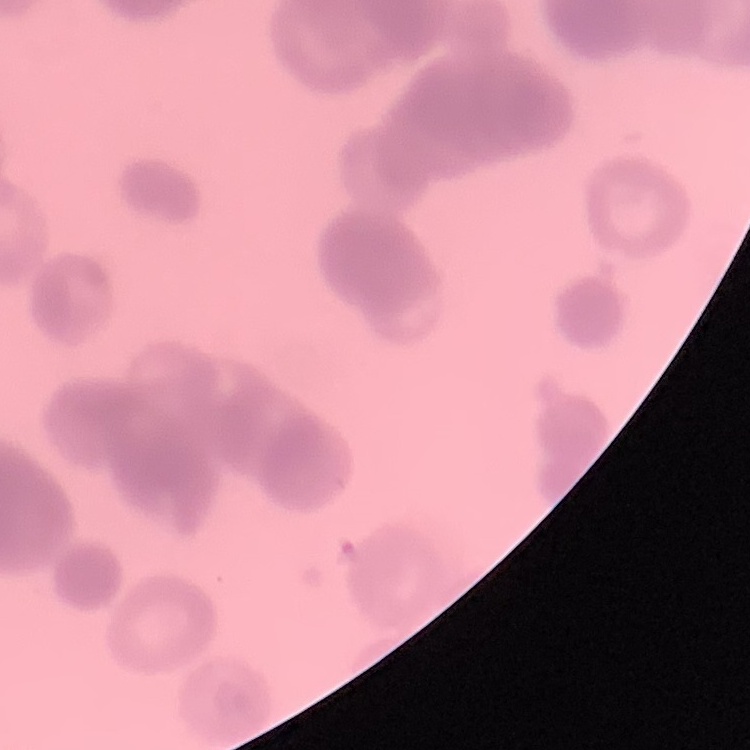
{
  "red_blood_cell_morphology": "rouleaux formation",
  "stain": "Field's or Giemsa",
  "preparation": "thin blood film",
  "image_type": "one tile cut from a larger photomicrograph"
}